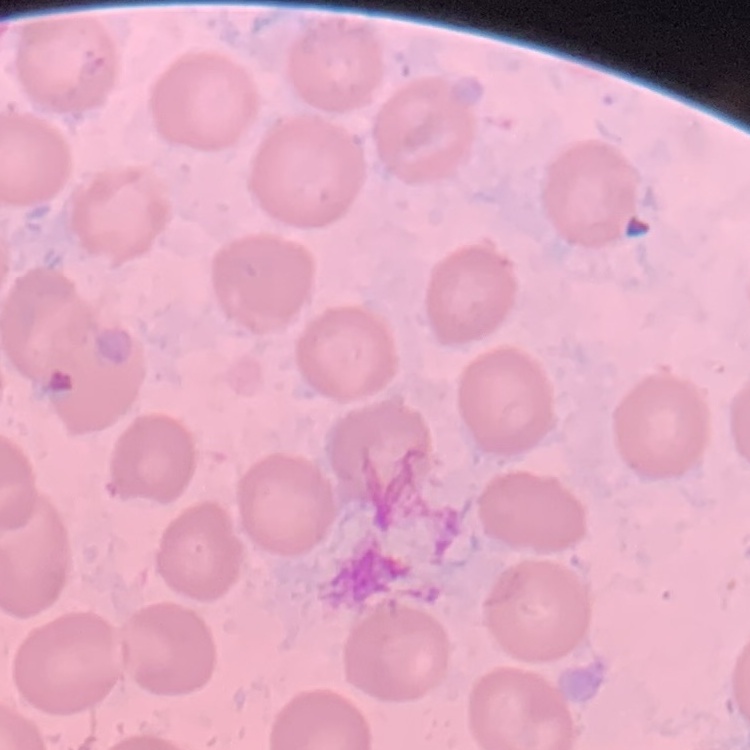

red blood cell morphology = no rouleaux formation
preparation = thin peripheral smear
image type = square crop of a larger photomicrograph
stain = Field's or Giemsa